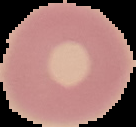

Summary:
  - Result: negative for Plasmodium parasites
  - Image type: segmented cell region with the area outside set to black
  - Preparation: thin blood smear
  - Image size: 136×127 pixels